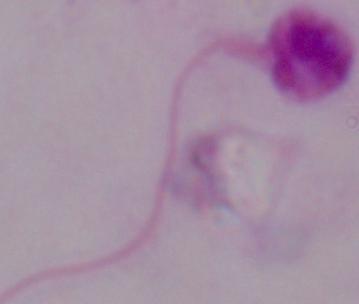 1000x magnification. Photomicrograph. A Leishmania parasite is shown.